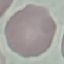
malaria status = uninfected
stain = Giemsa
image type = cell patch, automatically extracted from a larger field of view and resized to 64 × 64 pixels
capture = smartphone camera at the microscope eyepiece
preparation = thin blood film